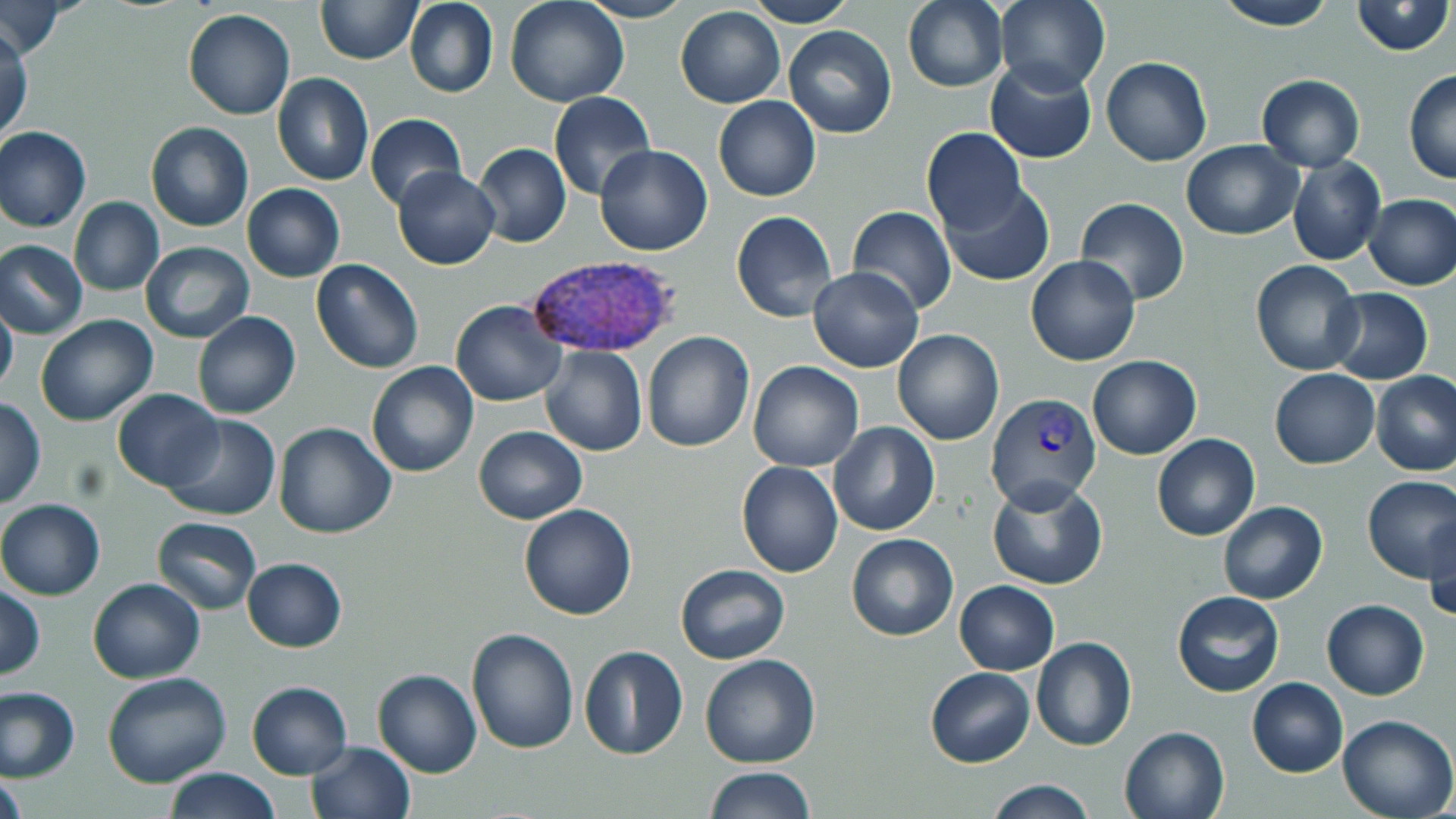
Summary:
  - Coordinate format: approximate bounding boxes as (x1, y1, x2, y2) in pixels
  - Uninfected red blood cell locations: (317, 0, 419, 63), (505, 0, 630, 107), (747, 0, 856, 26), (902, 0, 1009, 93), (993, 0, 1111, 95), (1212, 0, 1338, 31), (1350, 0, 1453, 56), (403, 1, 498, 98), (578, 1, 694, 23), (2, 4, 72, 57), (675, 6, 785, 109), (183, 8, 295, 121), (0, 24, 32, 145), (783, 25, 897, 139), (1101, 57, 1212, 166), (985, 58, 1098, 164), (1403, 69, 1456, 184), (272, 73, 374, 186), (1255, 74, 1366, 171), (549, 92, 657, 202), (714, 96, 821, 202), (364, 113, 467, 211), (145, 121, 253, 232), (1, 126, 92, 232), (921, 126, 1029, 234), (1181, 139, 1303, 240), (473, 143, 572, 248), (594, 145, 713, 256), (1287, 155, 1386, 267), (392, 167, 499, 270), (937, 180, 1054, 288), (242, 184, 345, 282), (1363, 193, 1456, 291), (68, 197, 164, 296), (1076, 197, 1189, 305), (847, 205, 957, 316), (731, 210, 837, 322), (1, 240, 89, 340), (139, 241, 254, 344), (1026, 255, 1140, 366), (310, 259, 424, 374), (1249, 259, 1364, 377), (808, 266, 925, 373), (1324, 288, 1433, 384), (0, 299, 18, 398), (451, 300, 565, 406), (191, 312, 300, 420), (35, 314, 158, 425), (893, 329, 1005, 446), (643, 331, 754, 452), (541, 347, 647, 457), (1086, 356, 1202, 459), (748, 360, 864, 471), (366, 362, 479, 477), (1269, 368, 1378, 469), (1371, 371, 1456, 476), (112, 389, 224, 492), (0, 398, 45, 509), (163, 414, 280, 522), (273, 422, 397, 538), (829, 422, 940, 535), (474, 426, 587, 524), (1152, 432, 1259, 541), (735, 461, 844, 579), (1360, 475, 1455, 581), (987, 477, 1109, 590), (0, 499, 105, 600), (1217, 501, 1327, 604), (518, 503, 637, 620), (1423, 510, 1456, 623), (152, 516, 261, 613), (846, 533, 959, 641), (242, 557, 347, 652), (675, 564, 789, 665), (87, 577, 207, 683), (954, 580, 1059, 674), (0, 586, 46, 680), (1170, 590, 1286, 697), (1322, 599, 1430, 700), (466, 628, 578, 755), (1030, 637, 1136, 751), (580, 645, 688, 759), (699, 654, 821, 769), (926, 667, 1034, 767), (372, 669, 482, 777), (103, 672, 233, 788), (1247, 677, 1348, 776), (247, 681, 352, 779), (1, 688, 80, 781), (1337, 714, 1455, 819), (1119, 724, 1231, 819), (307, 742, 415, 819), (706, 766, 815, 819), (164, 768, 280, 819), (1, 771, 28, 819), (983, 779, 1096, 819)
  - Plasmodium vivax-infected red blood cell locations: (524, 258, 680, 361), (986, 392, 1102, 511)
  - Slide-level diagnosis: Plasmodium vivax
  - Magnification: 1000x
  - Stain: May-Grünwald-Giemsa
  - Field of view: single
  - Modality: optical microscopy
  - Image size: 1456×819 pixels
  - Preparation: thin blood film